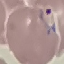
Summary:
  - Malaria status: parasitized
  - Image type: cell patch, automatically extracted from a larger field of view and resized to 64 × 64 pixels
  - Preparation: thin blood film
  - Capture: smartphone camera at the microscope eyepiece
  - Stain: Giemsa